Evaluate for Plasmodium parasites.
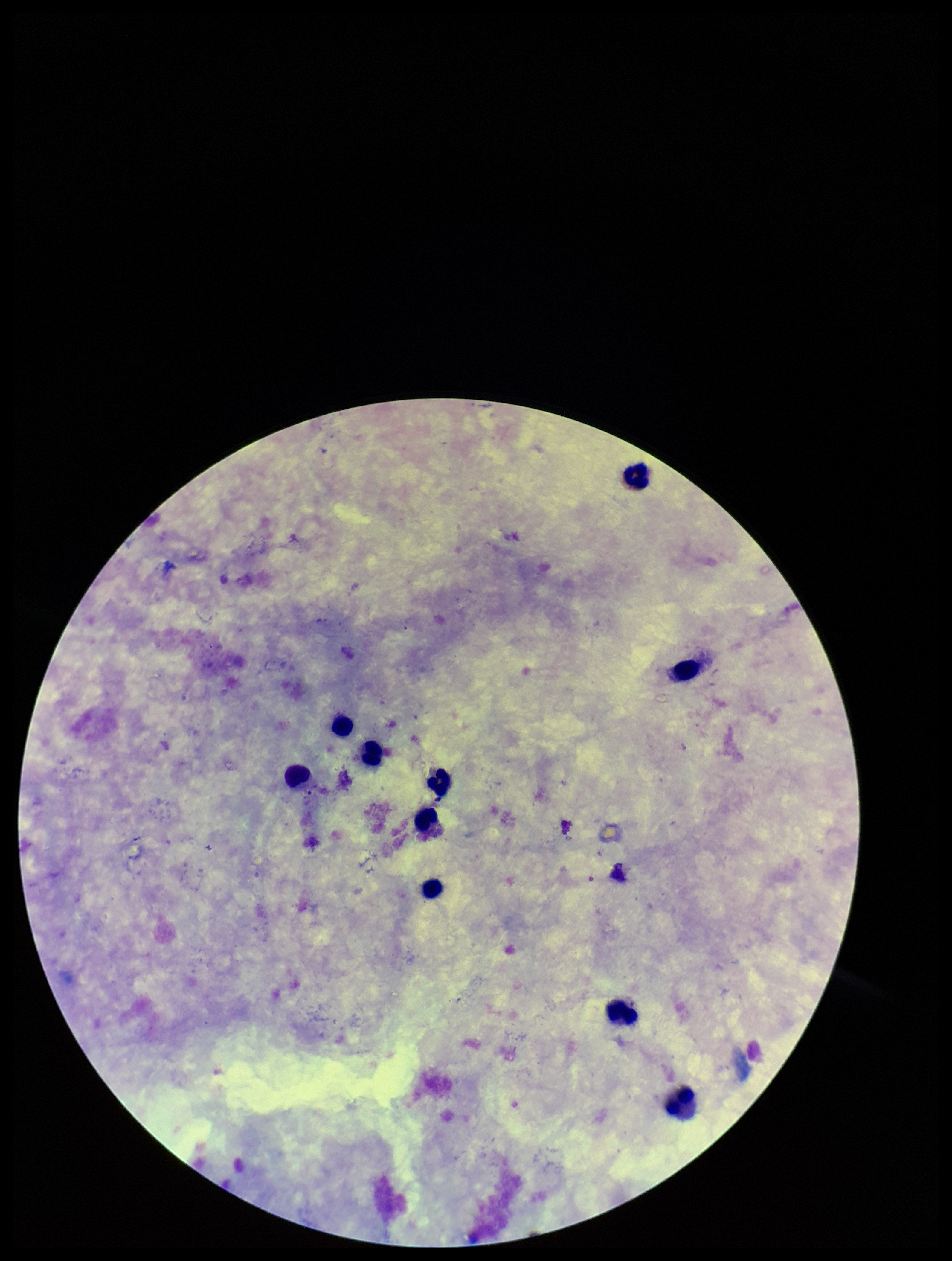

None seen.

Summary:
  - Stain: Giemsa
  - Patient malaria status: negative
  - Capture: smartphone photograph through the microscope eyepiece
  - Leukocyte count: 9
  - Preparation: thick blood smear
  - Field of view: one from this slide
  - Image size: 952×1261 pixels
  - Parasite count: 0